Classify this cell by malaria status.
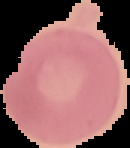

It is uninfected.

{
  "image_type": "segmented cell region on a black background",
  "image_size": "130×148 pixels",
  "preparation": "thin blood film"
}